Give the preparation type.
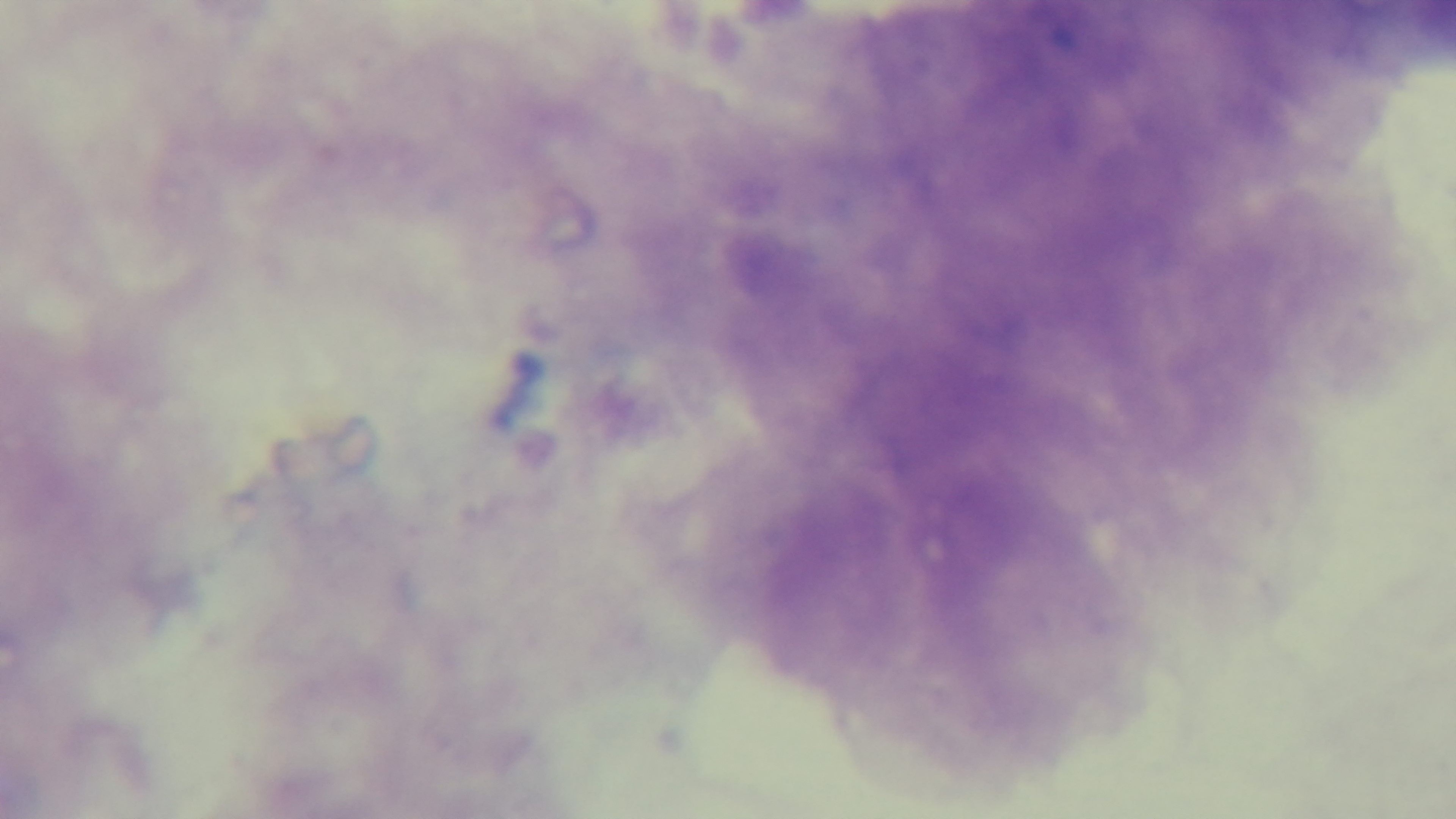
Thick.

stain: Giemsa
objective: 100x oil immersion
malaria_status: uninfected
modality: light microscopy
field_of_view: one from the slide
capture: mounted 4K digital camera